Report the malaria status of this cell.
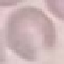
It is uninfected.

Summary:
  - Image type: cell patch, automatically extracted from a larger field of view and resized to 64 × 64 pixels
  - Preparation: thin blood film
  - Stain: Giemsa
  - Capture: smartphone through the microscope eyepiece